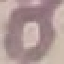

malaria status = uninfected
image type = cell patch, automatically extracted from a larger field of view and resized to 64 × 64 pixels
stain = Giemsa
preparation = thin blood film
capture = smartphone through the microscope eyepiece